Identify the parasite.
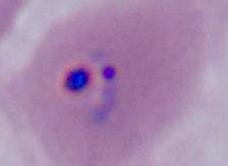
This is Plasmodium.

Summary:
  - Modality: photomicrograph
  - Magnification: 400x or 1000x